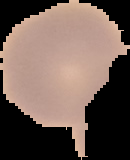 From a thin blood smear. Result: negative for malaria parasites. The area outside the segmented cell region is set to black. Image is 130×160 pixels.